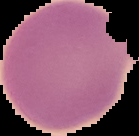

{
  "image_type": "segmented cell region on a black background",
  "image_size": "139×136 pixels",
  "malaria_status": "uninfected",
  "preparation": "thin blood film"
}